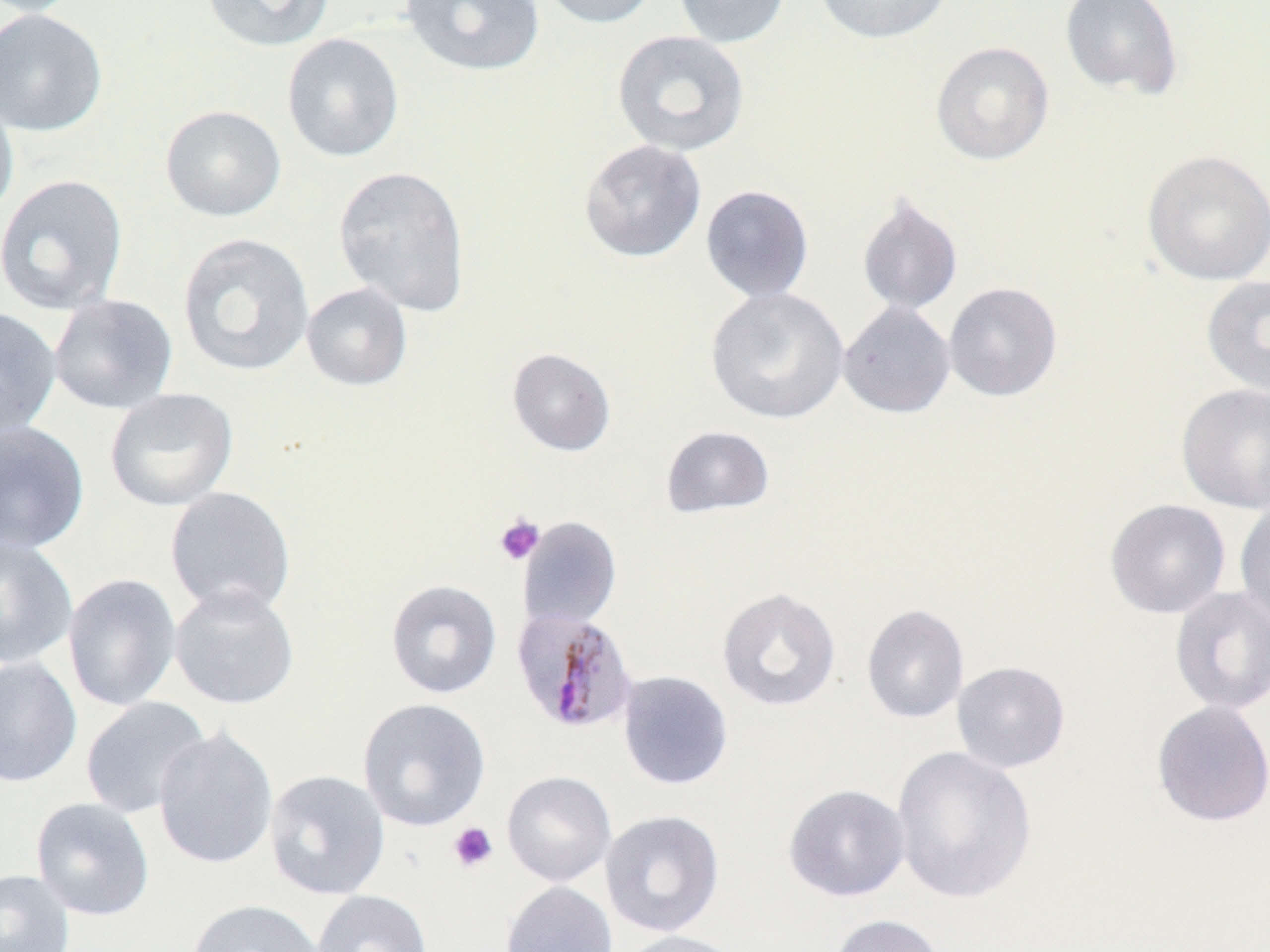
Plasmodium malariae-infected red blood cell locations = approximate bounding boxes as named x1/y1/x2/y2 corners in pixels: (x1=512, y1=607, x2=639, y2=734)
slide-level diagnosis = Plasmodium malariae
image size = 1270×952 pixels
platelet locations = approximate bounding boxes as named x1/y1/x2/y2 corners in pixels: (x1=494, y1=514, x2=545, y2=566), (x1=448, y1=822, x2=498, y2=873)
uninfected red blood cell locations = approximate bounding boxes as named x1/y1/x2/y2 corners in pixels: (x1=1, y1=0, x2=85, y2=17), (x1=201, y1=0, x2=335, y2=52), (x1=400, y1=0, x2=545, y2=76), (x1=535, y1=0, x2=661, y2=29), (x1=673, y1=0, x2=790, y2=49), (x1=813, y1=0, x2=955, y2=44), (x1=1060, y1=0, x2=1184, y2=101), (x1=0, y1=8, x2=108, y2=137), (x1=613, y1=30, x2=750, y2=156), (x1=282, y1=33, x2=404, y2=163), (x1=931, y1=41, x2=1054, y2=166), (x1=0, y1=89, x2=19, y2=222), (x1=160, y1=105, x2=286, y2=222), (x1=579, y1=139, x2=707, y2=263), (x1=1141, y1=149, x2=1270, y2=286), (x1=333, y1=165, x2=471, y2=316), (x1=0, y1=174, x2=129, y2=315), (x1=700, y1=184, x2=815, y2=303), (x1=857, y1=193, x2=963, y2=315), (x1=177, y1=233, x2=314, y2=377), (x1=1201, y1=274, x2=1270, y2=398), (x1=943, y1=282, x2=1062, y2=401), (x1=301, y1=283, x2=413, y2=391), (x1=705, y1=286, x2=849, y2=425), (x1=48, y1=294, x2=178, y2=414), (x1=838, y1=300, x2=956, y2=418), (x1=0, y1=306, x2=62, y2=438), (x1=507, y1=347, x2=616, y2=456), (x1=1176, y1=383, x2=1270, y2=513), (x1=104, y1=388, x2=239, y2=511), (x1=0, y1=420, x2=90, y2=554), (x1=660, y1=425, x2=775, y2=519), (x1=164, y1=486, x2=296, y2=618), (x1=1105, y1=499, x2=1231, y2=618), (x1=1234, y1=499, x2=1270, y2=628), (x1=518, y1=517, x2=622, y2=631), (x1=0, y1=534, x2=78, y2=669), (x1=62, y1=573, x2=182, y2=711), (x1=385, y1=579, x2=502, y2=699), (x1=169, y1=583, x2=300, y2=710), (x1=1169, y1=586, x2=1270, y2=715), (x1=717, y1=587, x2=842, y2=712), (x1=861, y1=603, x2=970, y2=724), (x1=0, y1=655, x2=83, y2=788), (x1=951, y1=661, x2=1071, y2=773), (x1=617, y1=670, x2=734, y2=791), (x1=80, y1=696, x2=212, y2=819), (x1=357, y1=698, x2=491, y2=832), (x1=1151, y1=700, x2=1270, y2=827), (x1=153, y1=726, x2=279, y2=870), (x1=890, y1=745, x2=1037, y2=905), (x1=264, y1=769, x2=390, y2=901), (x1=501, y1=771, x2=617, y2=886), (x1=783, y1=784, x2=910, y2=902), (x1=30, y1=797, x2=155, y2=921), (x1=599, y1=810, x2=725, y2=937), (x1=0, y1=869, x2=75, y2=952), (x1=500, y1=880, x2=617, y2=952), (x1=312, y1=889, x2=432, y2=952), (x1=186, y1=898, x2=325, y2=952), (x1=829, y1=914, x2=947, y2=952), (x1=614, y1=929, x2=747, y2=952)
modality = light microscopy
stain = May-Grünwald-Giemsa
preparation = thin blood film
magnification = 1000x
field of view = one of a larger specimen